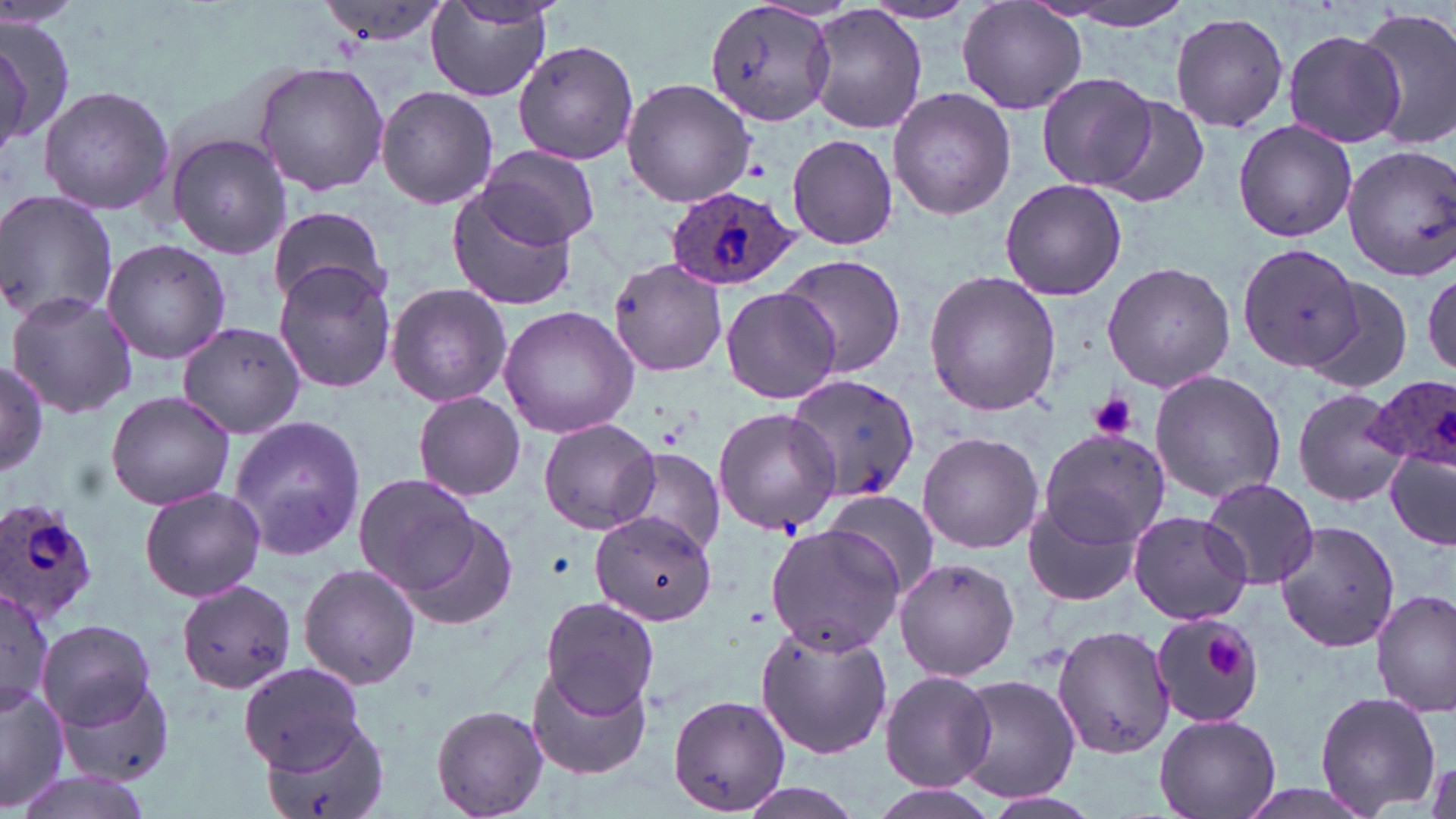
Summary:
  - Coordinate format: approximate bounding boxes as named x1/y1/x2/y2 corners in pixels
  - Plasmodium ovale-infected red blood cell locations: (x1=664, y1=188, x2=799, y2=289), (x1=1367, y1=375, x2=1456, y2=475), (x1=0, y1=497, x2=100, y2=628)
  - Platelet locations: (x1=1089, y1=392, x2=1138, y2=441), (x1=1206, y1=634, x2=1246, y2=678)
  - Uninfected red blood cell locations: (x1=425, y1=0, x2=555, y2=101), (x1=1040, y1=0, x2=1198, y2=30), (x1=316, y1=1, x2=454, y2=47), (x1=703, y1=1, x2=838, y2=130), (x1=863, y1=1, x2=975, y2=24), (x1=957, y1=1, x2=1088, y2=116), (x1=1353, y1=5, x2=1456, y2=151), (x1=805, y1=6, x2=926, y2=135), (x1=1170, y1=11, x2=1289, y2=132), (x1=0, y1=20, x2=75, y2=151), (x1=1282, y1=28, x2=1406, y2=149), (x1=512, y1=39, x2=639, y2=166), (x1=251, y1=61, x2=390, y2=195), (x1=1038, y1=75, x2=1158, y2=192), (x1=622, y1=78, x2=755, y2=207), (x1=35, y1=85, x2=173, y2=215), (x1=377, y1=86, x2=498, y2=209), (x1=887, y1=87, x2=1017, y2=220), (x1=1098, y1=96, x2=1210, y2=208), (x1=1232, y1=119, x2=1358, y2=243), (x1=165, y1=131, x2=293, y2=259), (x1=786, y1=134, x2=898, y2=249), (x1=1343, y1=145, x2=1455, y2=281), (x1=479, y1=146, x2=600, y2=249), (x1=999, y1=178, x2=1128, y2=301), (x1=447, y1=186, x2=582, y2=312), (x1=0, y1=190, x2=116, y2=326), (x1=266, y1=204, x2=390, y2=311), (x1=102, y1=239, x2=230, y2=363), (x1=1238, y1=244, x2=1360, y2=372), (x1=774, y1=252, x2=908, y2=377), (x1=606, y1=257, x2=728, y2=377), (x1=272, y1=261, x2=398, y2=393), (x1=1101, y1=261, x2=1236, y2=394), (x1=923, y1=271, x2=1062, y2=417), (x1=1303, y1=278, x2=1415, y2=397), (x1=386, y1=284, x2=512, y2=407), (x1=719, y1=284, x2=843, y2=405), (x1=6, y1=291, x2=135, y2=418), (x1=499, y1=306, x2=638, y2=437), (x1=175, y1=322, x2=308, y2=439), (x1=0, y1=362, x2=49, y2=477), (x1=1149, y1=369, x2=1287, y2=504), (x1=787, y1=372, x2=922, y2=502), (x1=1293, y1=386, x2=1407, y2=508), (x1=105, y1=390, x2=236, y2=511), (x1=409, y1=393, x2=527, y2=500), (x1=712, y1=407, x2=842, y2=535), (x1=226, y1=415, x2=369, y2=562), (x1=539, y1=418, x2=661, y2=535), (x1=1035, y1=428, x2=1170, y2=549), (x1=918, y1=431, x2=1041, y2=552), (x1=159, y1=444, x2=346, y2=586), (x1=613, y1=447, x2=726, y2=555), (x1=1384, y1=450, x2=1456, y2=550), (x1=353, y1=473, x2=483, y2=595), (x1=1202, y1=477, x2=1319, y2=590), (x1=138, y1=485, x2=266, y2=603), (x1=821, y1=489, x2=940, y2=600), (x1=1023, y1=499, x2=1141, y2=607), (x1=387, y1=504, x2=521, y2=632), (x1=590, y1=510, x2=717, y2=626), (x1=1127, y1=510, x2=1254, y2=626), (x1=1274, y1=521, x2=1401, y2=652), (x1=764, y1=523, x2=904, y2=653), (x1=892, y1=558, x2=1020, y2=681), (x1=297, y1=562, x2=420, y2=690), (x1=176, y1=580, x2=298, y2=695), (x1=0, y1=581, x2=55, y2=717), (x1=1373, y1=589, x2=1455, y2=717), (x1=541, y1=595, x2=660, y2=716), (x1=1149, y1=611, x2=1267, y2=728), (x1=39, y1=617, x2=158, y2=733), (x1=755, y1=620, x2=894, y2=761), (x1=1053, y1=621, x2=1174, y2=759), (x1=238, y1=662, x2=368, y2=776), (x1=526, y1=664, x2=654, y2=782), (x1=51, y1=670, x2=179, y2=789), (x1=879, y1=670, x2=996, y2=790), (x1=947, y1=675, x2=1082, y2=806), (x1=0, y1=682, x2=71, y2=813), (x1=1314, y1=689, x2=1441, y2=816), (x1=669, y1=694, x2=790, y2=816), (x1=429, y1=704, x2=550, y2=817), (x1=1155, y1=713, x2=1282, y2=819), (x1=257, y1=715, x2=391, y2=819), (x1=13, y1=766, x2=154, y2=819), (x1=730, y1=781, x2=868, y2=819), (x1=974, y1=789, x2=1104, y2=819)
  - Slide-level diagnosis: Plasmodium ovale
  - Field of view: single
  - Image size: 1456×819 pixels
  - Magnification: 1000x
  - Modality: optical microscopy
  - Stain: May-Grünwald-Giemsa
  - Preparation: thin blood smear